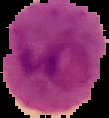

preparation: thin blood smear
image_type: cell region segmented out of the field of view; surrounding area masked to black
malaria_status: parasitized
image_size: 109×118 pixels